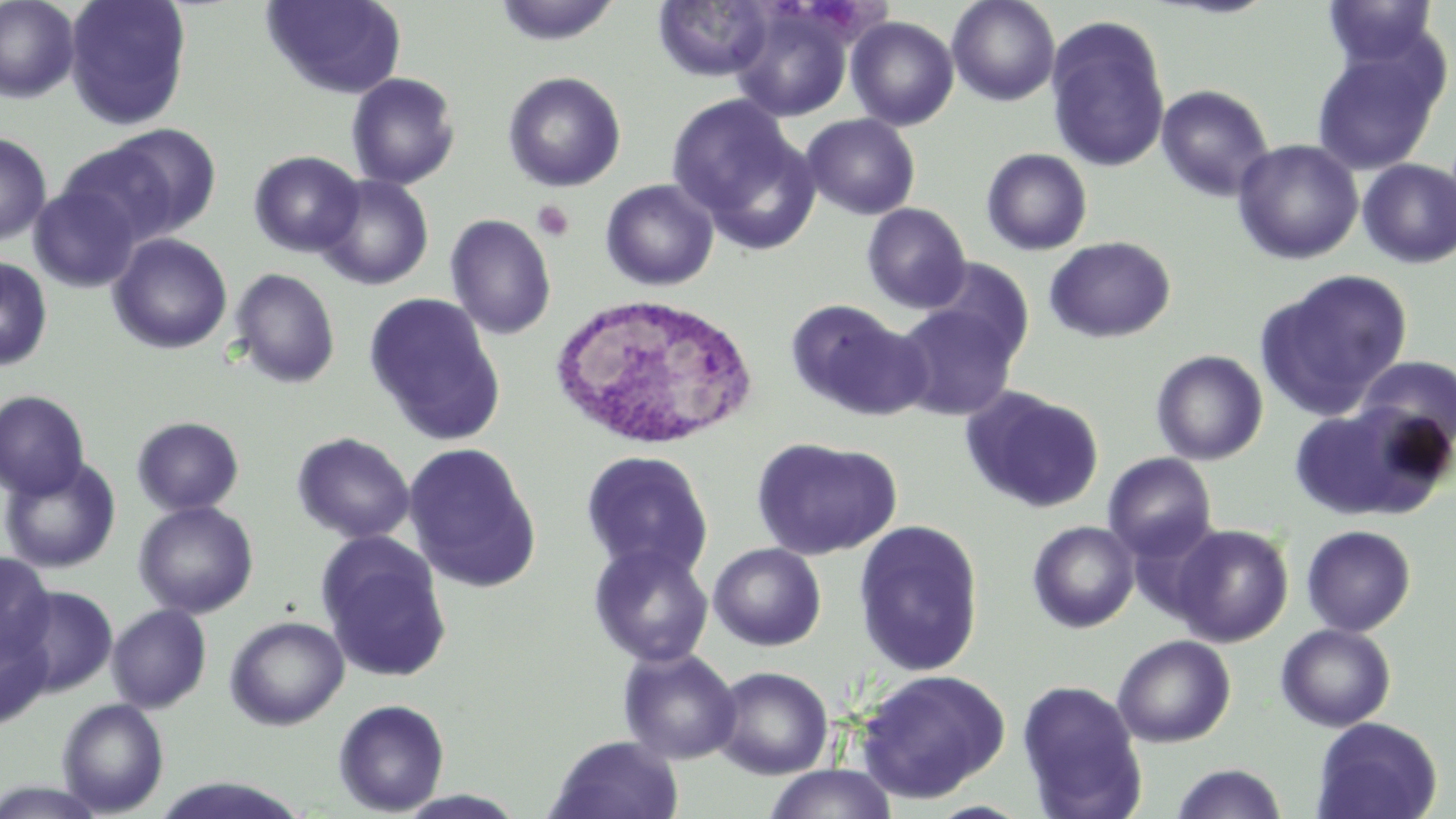

Summary:
  - Coordinate format: approximate bounding boxes as [x1, y1, x2, y2] in pixels
  - White blood cell locations: [545, 291, 759, 452]
  - Platelet locations: [533, 200, 575, 241]
  - Uninfected red blood cell locations: [0, 0, 80, 103], [64, 0, 192, 130], [261, 0, 407, 98], [493, 0, 623, 47], [653, 0, 775, 81], [947, 0, 1061, 106], [1158, 0, 1281, 19], [1321, 0, 1441, 70], [730, 6, 852, 122], [1046, 15, 1171, 173], [846, 16, 959, 131], [1312, 45, 1446, 174], [503, 71, 626, 192], [346, 72, 461, 190], [1156, 84, 1274, 201], [665, 93, 800, 226], [801, 114, 921, 220], [106, 123, 222, 237], [0, 132, 52, 245], [1233, 139, 1364, 265], [56, 142, 182, 246], [981, 148, 1092, 255], [249, 151, 365, 257], [1358, 158, 1456, 268], [315, 175, 434, 290], [601, 179, 719, 291], [29, 183, 141, 293], [861, 203, 971, 314], [445, 214, 558, 340], [108, 233, 233, 354], [1044, 236, 1175, 343], [0, 256, 53, 372], [927, 259, 1034, 364], [229, 268, 340, 389], [1258, 268, 1412, 418], [364, 292, 505, 444], [786, 300, 927, 419], [894, 303, 1019, 420], [1151, 349, 1268, 466], [1353, 355, 1456, 454], [960, 386, 1105, 514], [0, 390, 90, 500], [1287, 404, 1433, 521], [131, 416, 245, 516], [292, 432, 415, 544], [751, 437, 902, 561], [403, 443, 541, 592], [580, 450, 713, 579], [1104, 453, 1217, 560], [0, 457, 121, 573], [133, 500, 259, 619], [853, 519, 985, 676], [1027, 521, 1140, 633], [1169, 524, 1293, 646], [1301, 525, 1416, 636], [317, 535, 453, 683], [588, 542, 714, 668], [708, 542, 827, 651], [0, 551, 56, 664], [11, 584, 117, 696], [107, 604, 211, 713], [225, 616, 349, 730], [0, 619, 53, 728], [1276, 623, 1396, 731], [1112, 634, 1236, 747], [618, 648, 742, 764], [712, 666, 834, 780], [855, 668, 1012, 803], [1017, 679, 1147, 819], [57, 698, 169, 816], [333, 699, 450, 816], [1310, 716, 1442, 819], [546, 735, 685, 818], [1170, 763, 1288, 819], [762, 764, 899, 819], [146, 775, 313, 818], [395, 789, 528, 818]
  - Slide-level diagnosis: no evidence of blood parasites
  - Modality: light microscopy
  - Magnification: 1000x
  - Image size: 1456×819 pixels
  - Stain: May-Grünwald-Giemsa
  - Field of view: single
  - Preparation: thin blood smear